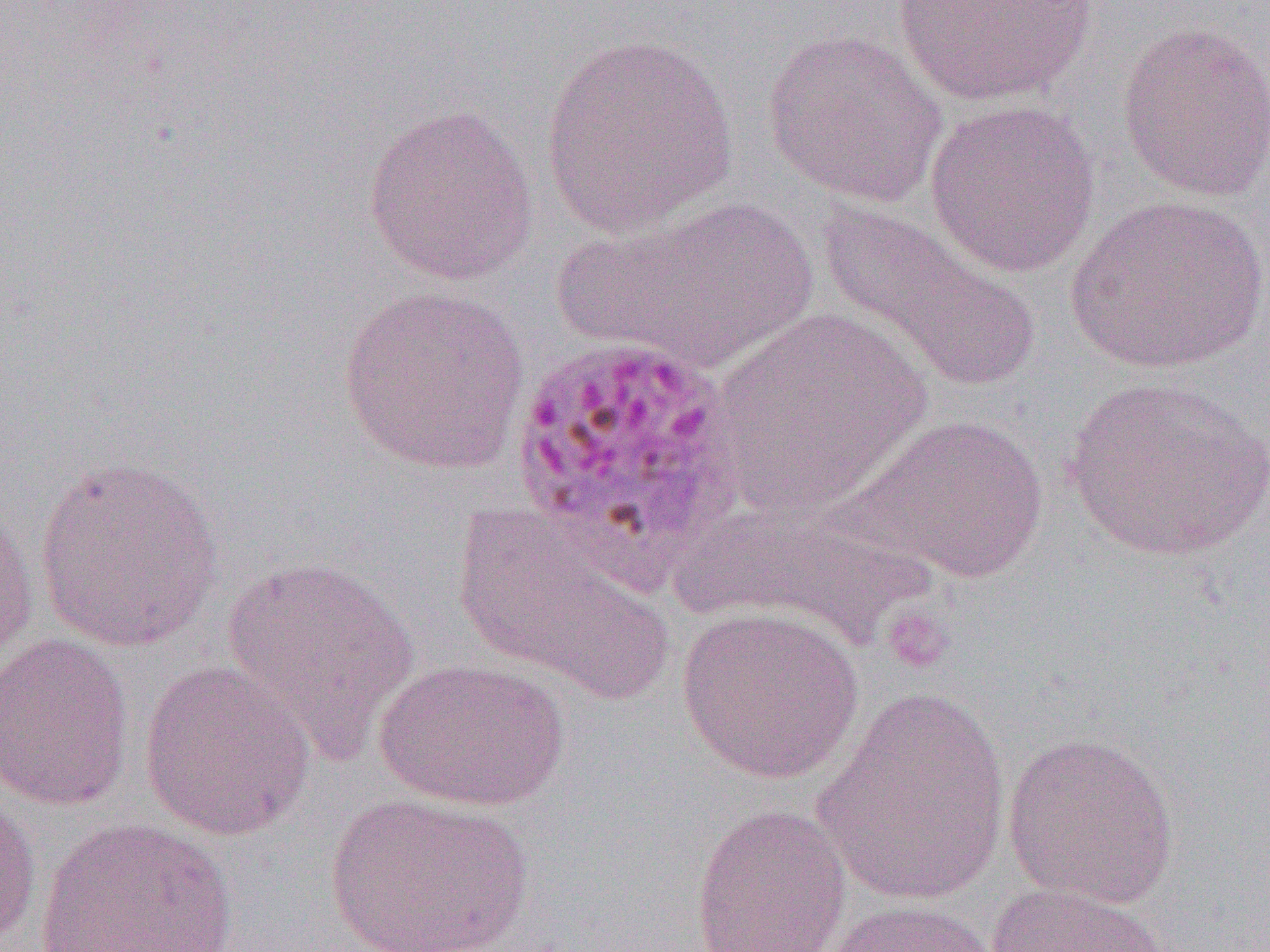
Approximate bounding boxes as (x1, y1, x2, y2) in pixels. Uninfected red blood cell locations: (887, 0, 1104, 107), (1115, 19, 1270, 202), (762, 28, 947, 208), (539, 34, 739, 238), (924, 98, 1101, 277), (362, 102, 539, 288), (560, 194, 820, 376), (1065, 194, 1270, 374), (815, 199, 1042, 396), (337, 284, 531, 476), (713, 309, 932, 514), (1062, 373, 1270, 561), (840, 411, 1053, 584), (33, 454, 226, 651), (666, 495, 942, 652), (454, 504, 675, 707), (0, 505, 39, 668), (221, 554, 423, 759), (677, 606, 863, 784), (0, 632, 135, 811), (373, 658, 570, 811), (139, 659, 316, 842), (812, 686, 1012, 909), (1002, 730, 1180, 909), (0, 788, 41, 950), (325, 790, 534, 951), (690, 803, 851, 952), (34, 816, 239, 952), (985, 880, 1174, 952), (822, 899, 1007, 952). Platelet locations: (879, 604, 955, 673). Plasmodium ovale-infected red blood cell locations: (507, 331, 749, 581). Slide-level diagnosis: Plasmodium ovale. Image is 1270×952 pixels. Single field of view. 1000x magnification. Thin blood film. Light microscopy.